Identify the cell.
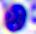
A leukocyte.

magnification: 400x
modality: photomicrograph